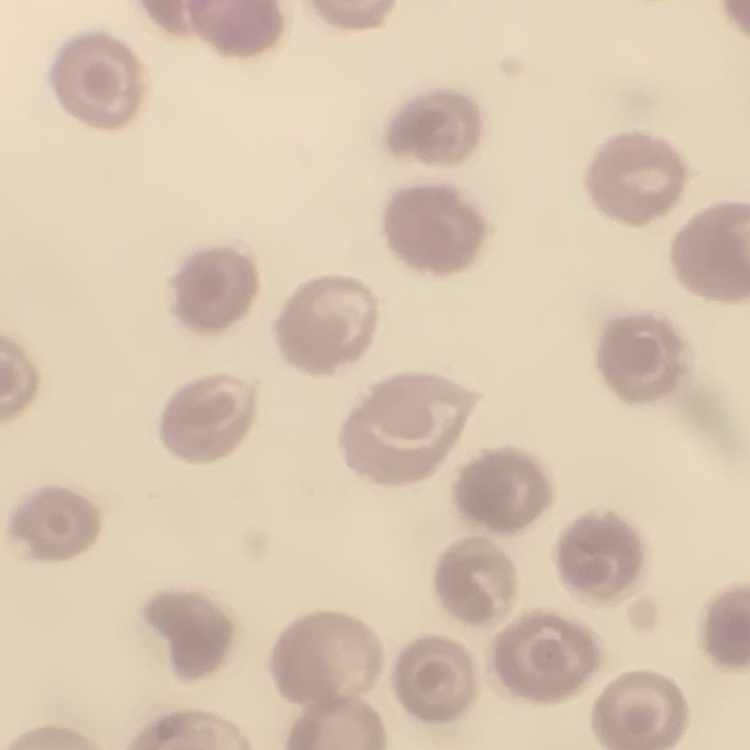
erythrocyte morphology = no rouleaux formation
image type = square crop of a larger photomicrograph
preparation = thin blood film
stain = Field's or Giemsa